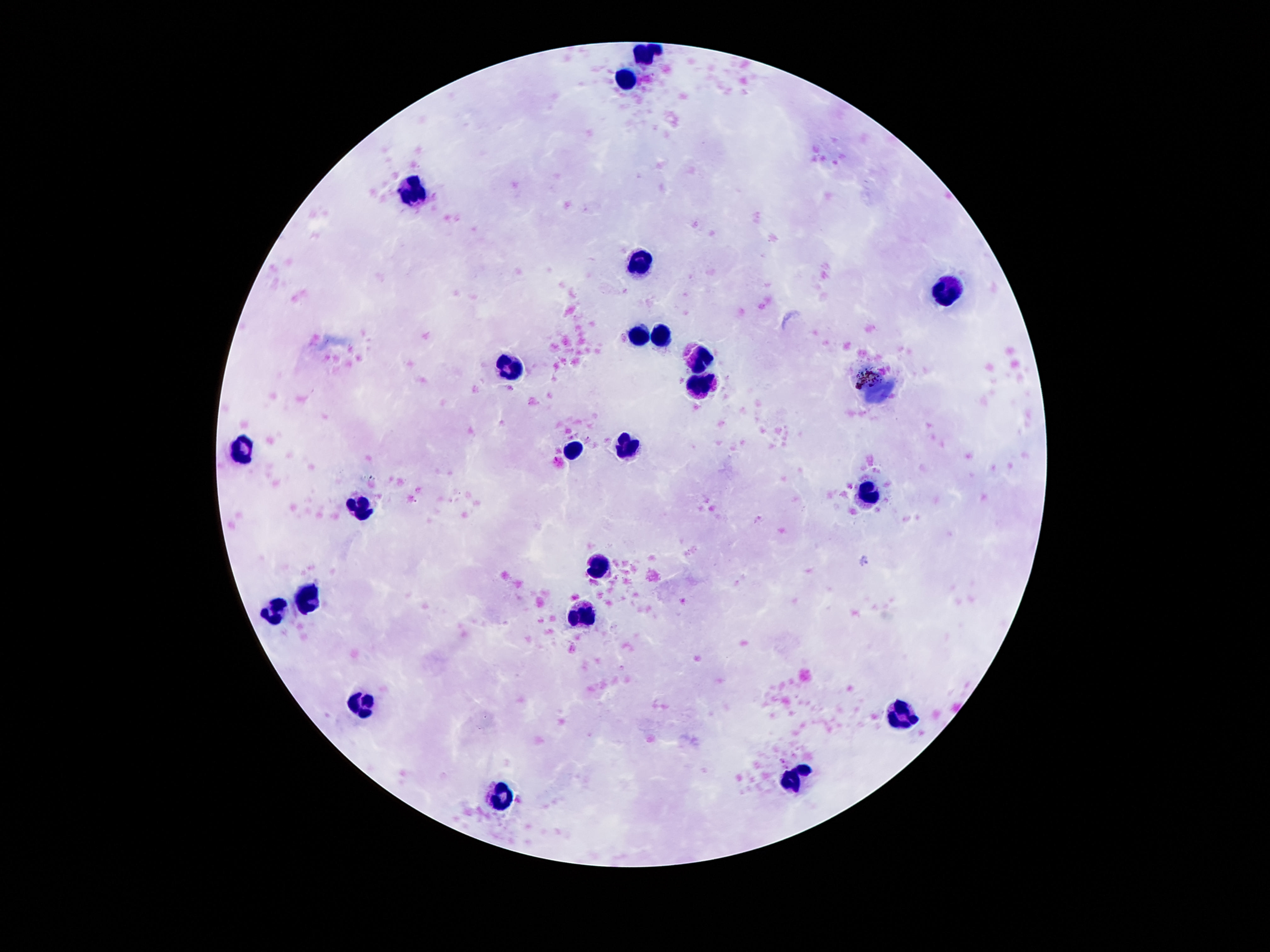
Approximate centers as {x, y} in pixels. Leukocyte locations: {648, 56}, {627, 79}, {412, 188}, {641, 264}, {948, 292}, {636, 335}, {659, 337}, {700, 360}, {509, 366}, {702, 385}, {879, 394}, {627, 449}, {246, 450}, {575, 451}, {866, 498}, {362, 505}, {599, 564}, {308, 598}, {276, 612}, {581, 616}, {363, 703}, {901, 717}, {798, 780}, {503, 796}. Patient malaria status: not infected. Single field of view. Thick blood film. Photographed through the microscope eyepiece with a smartphone camera. Giemsa stain. Image is 1270×952 pixels. 100x magnification.